Give the extent of all Plasmodium malariae-infected red blood cells.
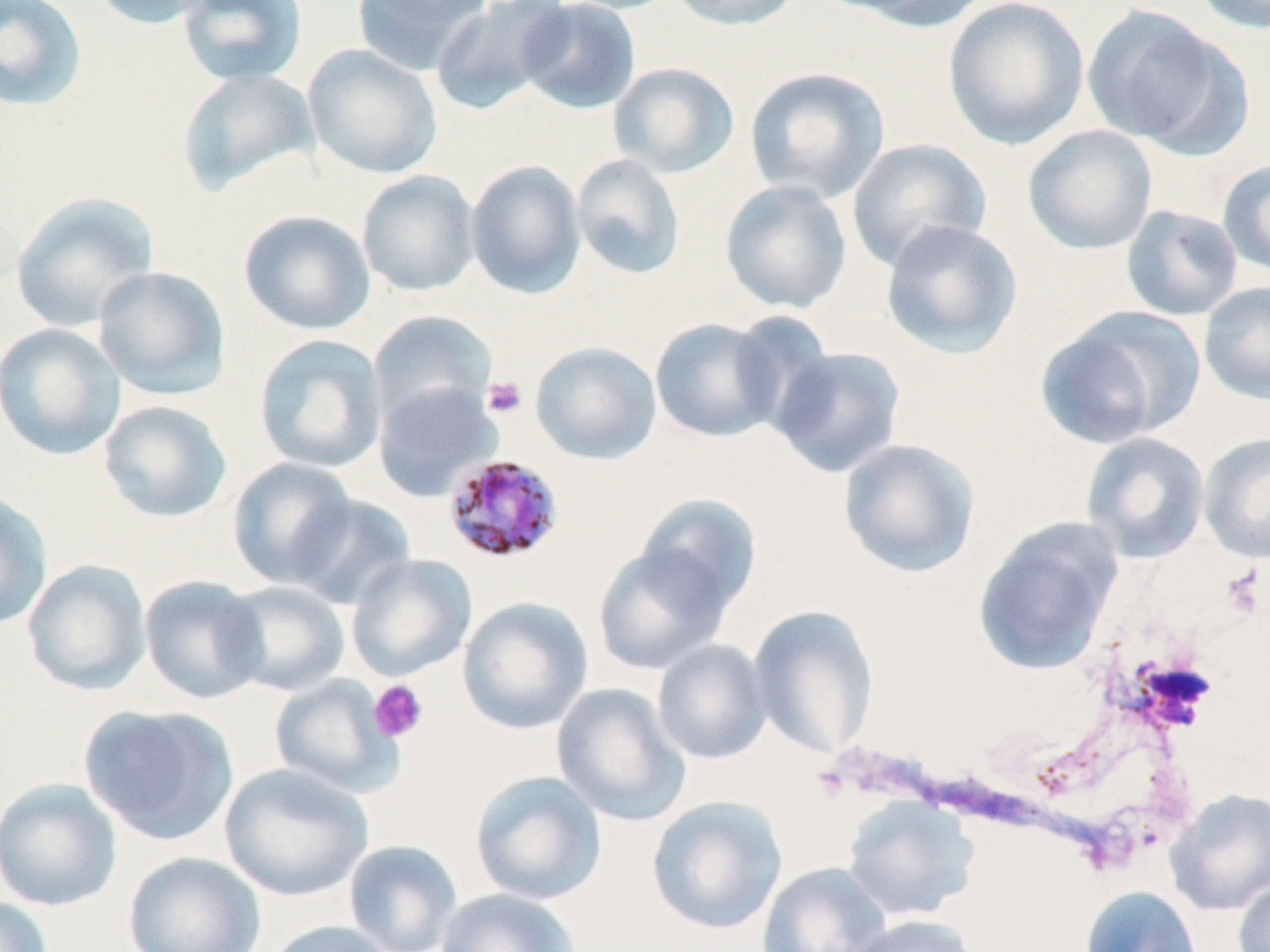
Approximate bounding boxes as (x1, y1, x2, y2) in pixels.
Plasmodium malariae-infected red blood cells: (441, 454, 565, 565).

slide-level diagnosis = Plasmodium malariae
uninfected red blood cell locations = approximate bounding boxes as (x1, y1, x2, y2) in pixels: (0, 0, 88, 111), (89, 0, 218, 30), (176, 0, 307, 87), (352, 0, 492, 75), (429, 0, 573, 114), (546, 0, 685, 15), (667, 0, 808, 31), (828, 0, 993, 31), (943, 0, 1090, 150), (1188, 0, 1270, 34), (516, 1, 642, 115), (1081, 4, 1242, 152), (304, 44, 443, 180), (608, 62, 739, 178), (744, 67, 890, 204), (176, 68, 320, 197), (1022, 125, 1158, 254), (846, 138, 992, 271), (570, 154, 687, 280), (1218, 157, 1270, 278), (465, 160, 586, 298), (357, 170, 481, 297), (720, 179, 853, 315), (9, 192, 160, 332), (1120, 204, 1244, 322), (239, 210, 375, 335), (880, 219, 1023, 360), (93, 266, 231, 400), (1198, 281, 1270, 406), (1035, 306, 1205, 451), (367, 310, 497, 429), (649, 318, 786, 443), (0, 323, 126, 460), (253, 334, 388, 474), (530, 341, 662, 464), (767, 346, 907, 479), (372, 380, 502, 501), (97, 399, 233, 524), (1198, 431, 1270, 564), (1079, 432, 1211, 564), (838, 437, 982, 579), (227, 458, 358, 589), (0, 491, 54, 631), (287, 494, 416, 611), (632, 495, 762, 619), (972, 516, 1125, 677), (593, 540, 734, 675), (346, 554, 477, 681), (22, 560, 152, 696), (139, 576, 267, 705), (217, 581, 350, 697), (457, 597, 593, 734), (748, 605, 880, 759), (652, 640, 773, 764), (268, 674, 402, 798), (552, 683, 691, 826), (79, 704, 239, 846), (219, 762, 374, 901), (469, 770, 608, 905), (0, 778, 123, 912), (1165, 788, 1270, 916), (646, 796, 788, 935), (842, 797, 980, 921), (343, 840, 463, 952), (122, 851, 266, 952), (757, 862, 890, 952), (1233, 873, 1269, 952), (1079, 885, 1203, 952), (434, 888, 580, 952), (0, 897, 55, 952), (844, 914, 980, 952), (262, 920, 398, 952)
modality = optical microscopy
stain = May-Grünwald-Giemsa
field of view = one of a larger specimen
platelet locations = approximate bounding boxes as (x1, y1, x2, y2) in pixels: (482, 376, 527, 417), (1221, 564, 1266, 621), (368, 679, 428, 743), (812, 763, 851, 801)
magnification = 1000x
image size = 1270×952 pixels
preparation = thin blood film